Locate and identify every blood parasite.
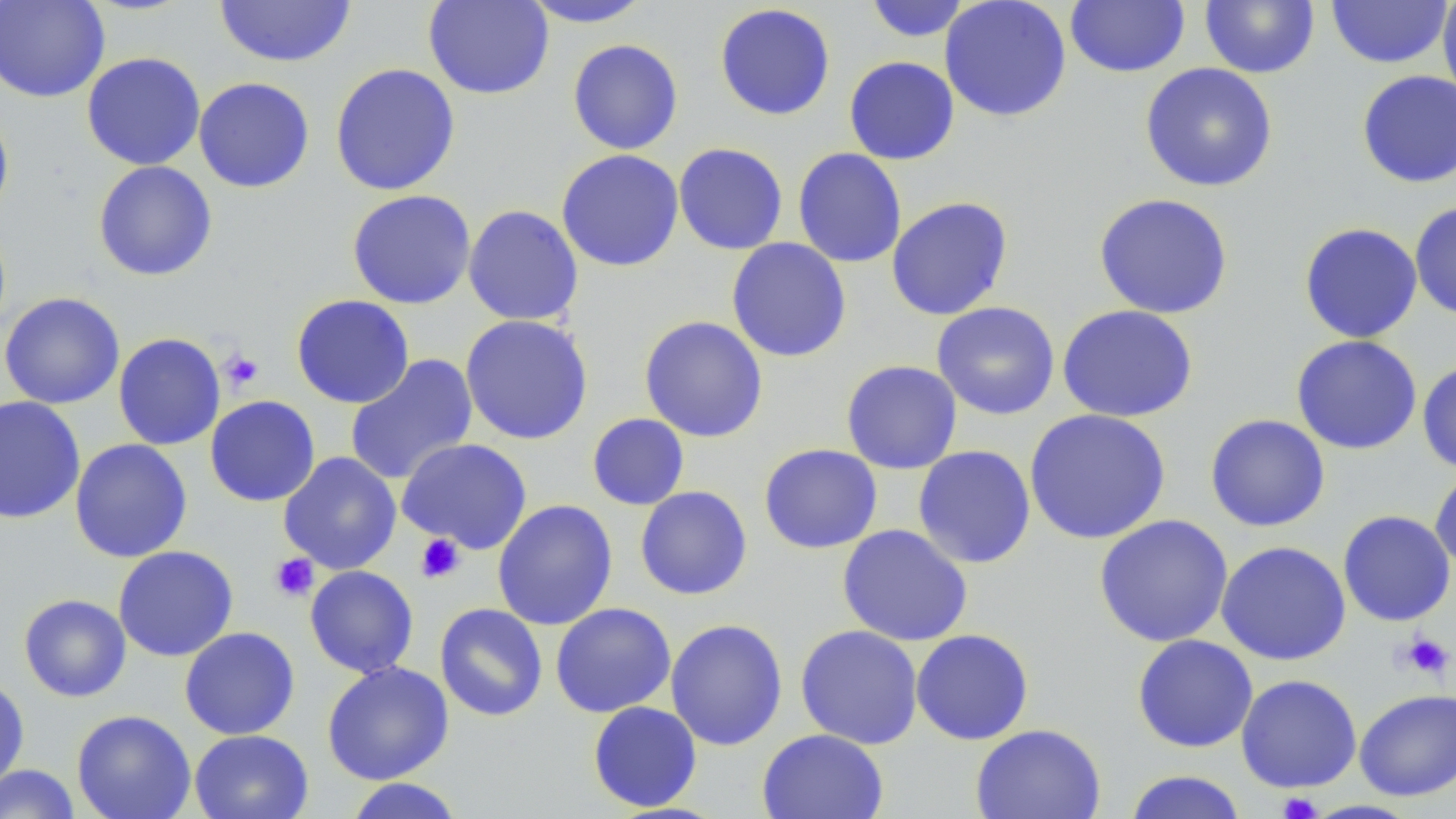

No blood parasites observed.

Summary:
  - Coordinate format: approximate bounding boxes as named x1/y1/x2/y2 corners in pixels
  - Platelet locations: (x1=220, y1=349, x2=265, y2=392), (x1=415, y1=533, x2=465, y2=583), (x1=269, y1=553, x2=319, y2=602), (x1=1400, y1=632, x2=1453, y2=679), (x1=1276, y1=791, x2=1323, y2=819)
  - Uninfected red blood cell locations: (x1=0, y1=0, x2=110, y2=102), (x1=214, y1=0, x2=357, y2=68), (x1=423, y1=0, x2=554, y2=99), (x1=519, y1=0, x2=656, y2=28), (x1=863, y1=0, x2=972, y2=42), (x1=939, y1=0, x2=1072, y2=122), (x1=1325, y1=0, x2=1453, y2=69), (x1=1437, y1=0, x2=1456, y2=107), (x1=1064, y1=1, x2=1190, y2=77), (x1=1199, y1=1, x2=1320, y2=78), (x1=714, y1=3, x2=836, y2=121), (x1=567, y1=39, x2=684, y2=155), (x1=81, y1=52, x2=206, y2=170), (x1=843, y1=56, x2=960, y2=165), (x1=1139, y1=62, x2=1278, y2=192), (x1=329, y1=63, x2=461, y2=197), (x1=1356, y1=69, x2=1456, y2=189), (x1=193, y1=76, x2=315, y2=193), (x1=0, y1=106, x2=14, y2=223), (x1=673, y1=142, x2=789, y2=255), (x1=792, y1=147, x2=907, y2=268), (x1=556, y1=149, x2=684, y2=272), (x1=93, y1=160, x2=217, y2=281), (x1=347, y1=189, x2=476, y2=309), (x1=1093, y1=192, x2=1234, y2=319), (x1=886, y1=195, x2=1014, y2=321), (x1=1409, y1=201, x2=1456, y2=321), (x1=463, y1=204, x2=584, y2=327), (x1=1298, y1=222, x2=1423, y2=343), (x1=726, y1=237, x2=852, y2=363), (x1=0, y1=292, x2=126, y2=409), (x1=291, y1=294, x2=415, y2=408), (x1=931, y1=302, x2=1060, y2=420), (x1=1057, y1=305, x2=1198, y2=423), (x1=459, y1=314, x2=594, y2=445), (x1=639, y1=315, x2=769, y2=443), (x1=112, y1=332, x2=226, y2=451), (x1=1290, y1=335, x2=1422, y2=455), (x1=344, y1=353, x2=479, y2=486), (x1=841, y1=359, x2=963, y2=474), (x1=1416, y1=360, x2=1456, y2=473), (x1=204, y1=395, x2=320, y2=507), (x1=0, y1=396, x2=86, y2=524), (x1=1023, y1=408, x2=1171, y2=545), (x1=586, y1=413, x2=690, y2=511), (x1=1205, y1=413, x2=1331, y2=532), (x1=69, y1=438, x2=192, y2=563), (x1=397, y1=438, x2=532, y2=554), (x1=758, y1=443, x2=883, y2=554), (x1=913, y1=445, x2=1036, y2=569), (x1=278, y1=451, x2=402, y2=574), (x1=1430, y1=467, x2=1456, y2=575), (x1=634, y1=485, x2=753, y2=600), (x1=492, y1=499, x2=618, y2=631), (x1=1337, y1=510, x2=1456, y2=627), (x1=1094, y1=514, x2=1233, y2=648), (x1=836, y1=524, x2=973, y2=646), (x1=1215, y1=540, x2=1352, y2=666), (x1=113, y1=545, x2=238, y2=662), (x1=304, y1=565, x2=419, y2=678), (x1=19, y1=594, x2=131, y2=702), (x1=550, y1=602, x2=676, y2=718), (x1=434, y1=603, x2=548, y2=721), (x1=665, y1=618, x2=788, y2=751), (x1=795, y1=624, x2=924, y2=749), (x1=179, y1=626, x2=300, y2=740), (x1=910, y1=629, x2=1034, y2=745), (x1=1131, y1=634, x2=1258, y2=753), (x1=321, y1=660, x2=454, y2=785), (x1=1235, y1=674, x2=1362, y2=793), (x1=0, y1=675, x2=29, y2=792), (x1=1354, y1=688, x2=1456, y2=801), (x1=586, y1=700, x2=703, y2=812), (x1=71, y1=709, x2=196, y2=819), (x1=970, y1=723, x2=1106, y2=819), (x1=757, y1=728, x2=889, y2=819), (x1=189, y1=729, x2=313, y2=819), (x1=0, y1=764, x2=81, y2=819), (x1=1123, y1=770, x2=1249, y2=819), (x1=342, y1=778, x2=467, y2=819)
  - Slide-level diagnosis: no evidence of blood parasites
  - Modality: optical microscopy
  - Field of view: one of a larger specimen
  - Magnification: 1000x
  - Preparation: thin blood smear
  - Stain: May-Grünwald-Giemsa
  - Image size: 1456×819 pixels